Give the position of every malaria parasite.
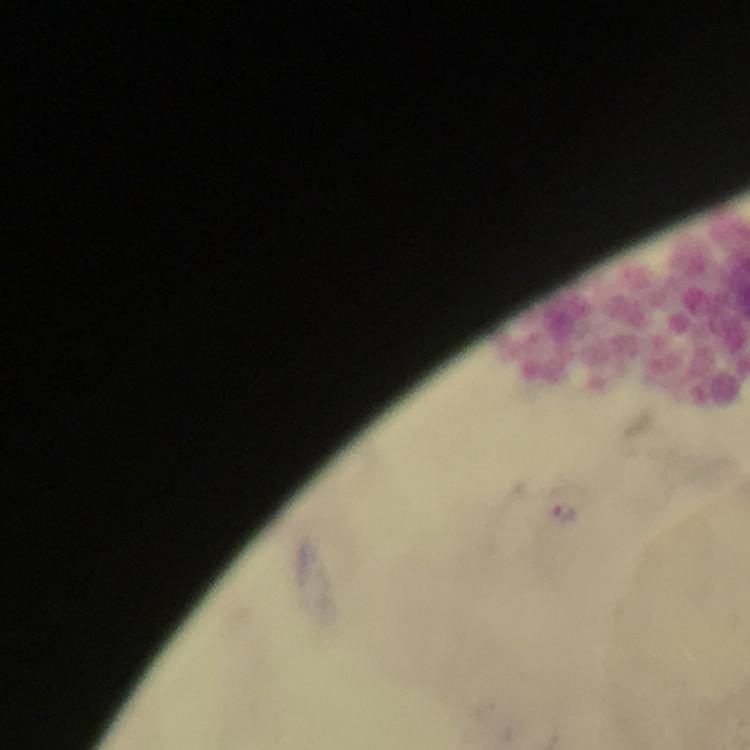
Approximate centers as (x, y) in pixels.
Malaria parasites: (563, 512).

A crop from one field of view. Thick smear. Immersion oil applied. Image is 750×750 pixels. From a malaria diagnostic workup. Giemsa-stained preparation. At 100x magnification. Photographed through the microscope with a smartphone camera.